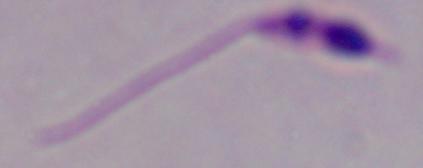

modality = photomicrograph
identification = Leishmania
magnification = 1000x